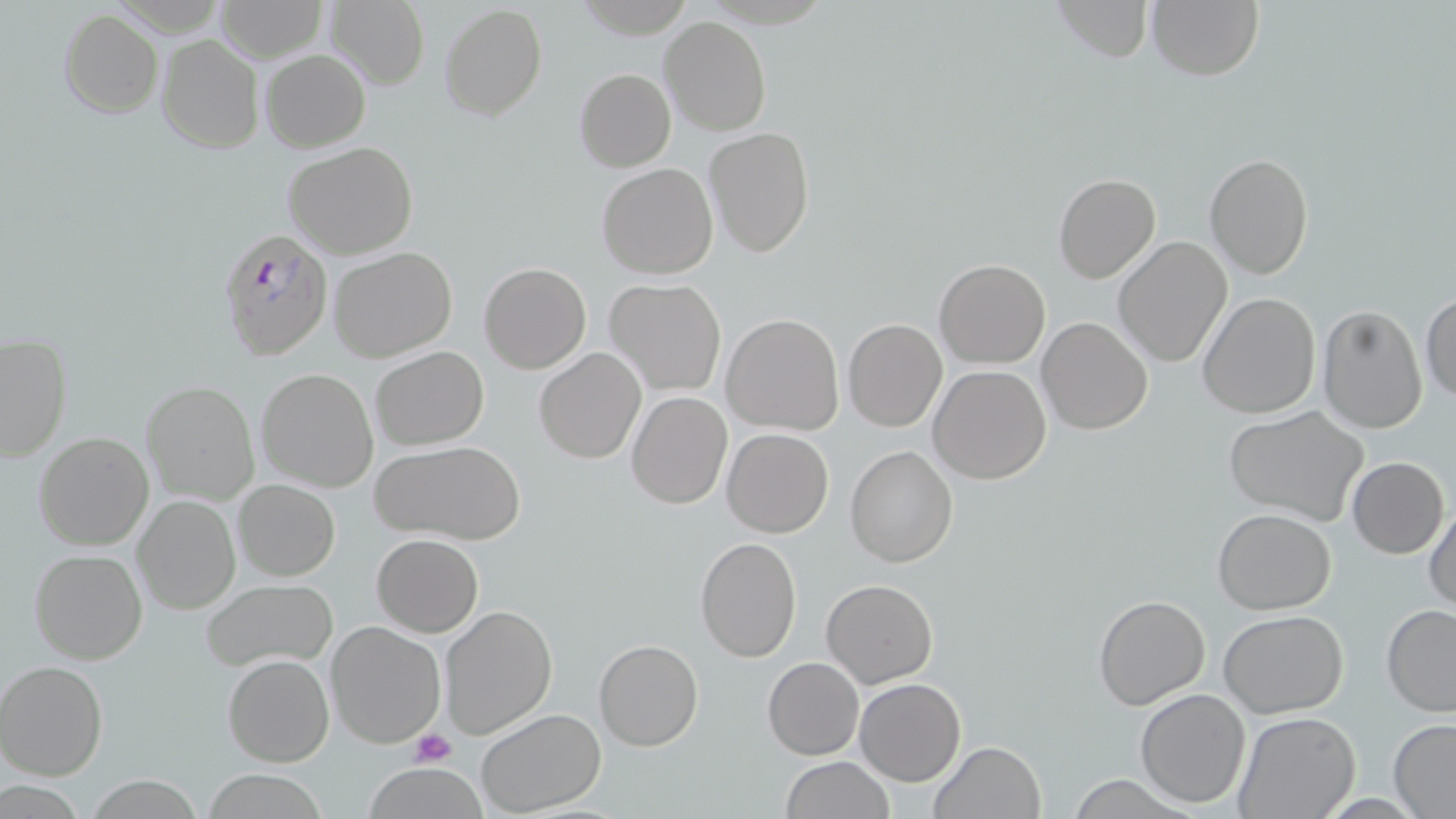

Summary:
  - Coordinate format: approximate bounding boxes as (x1, y1, x2, y2) in pixels
  - Uninfected red blood cell locations: (213, 0, 325, 60), (1050, 0, 1155, 63), (1146, 0, 1264, 81), (323, 1, 430, 88), (439, 3, 547, 122), (59, 9, 163, 118), (660, 16, 772, 136), (156, 35, 263, 154), (260, 48, 371, 152), (574, 68, 675, 173), (703, 127, 815, 260), (283, 141, 420, 260), (1205, 153, 1315, 280), (596, 164, 718, 280), (1053, 173, 1160, 283), (1112, 236, 1232, 367), (328, 247, 458, 363), (934, 259, 1051, 368), (479, 262, 591, 374), (604, 278, 726, 396), (1198, 292, 1321, 419), (1421, 292, 1455, 404), (1318, 305, 1428, 433), (721, 313, 844, 435), (1036, 316, 1153, 434), (843, 319, 947, 431), (1, 335, 72, 462), (371, 346, 489, 451), (534, 348, 646, 463), (928, 365, 1052, 483), (256, 368, 379, 493), (141, 382, 259, 505), (626, 391, 732, 509), (1225, 406, 1370, 527), (721, 427, 833, 537), (33, 431, 156, 551), (375, 440, 524, 547), (846, 446, 958, 566), (1347, 456, 1449, 558), (233, 479, 340, 582), (133, 494, 241, 616), (1424, 501, 1456, 615), (1213, 508, 1338, 614), (372, 534, 483, 636), (694, 536, 803, 662), (29, 547, 148, 665), (822, 577, 937, 688), (201, 579, 337, 672), (1093, 594, 1211, 711), (1381, 604, 1456, 715), (440, 605, 557, 739), (1219, 610, 1349, 717), (326, 621, 447, 749), (594, 639, 703, 751), (223, 654, 333, 767), (762, 657, 864, 760), (0, 660, 108, 781), (854, 679, 965, 786), (1135, 689, 1250, 806), (475, 708, 605, 816), (1233, 711, 1360, 818), (1387, 718, 1456, 816), (929, 740, 1048, 819), (780, 757, 893, 818), (360, 763, 491, 818), (203, 772, 326, 818)
  - Plasmodium falciparum-infected red blood cell locations: (219, 228, 332, 363)
  - Platelet locations: (409, 729, 456, 767)
  - Slide-level diagnosis: Plasmodium falciparum
  - Preparation: thin blood film
  - Field of view: single
  - Image size: 1456×819 pixels
  - Stain: May-Grünwald-Giemsa
  - Magnification: 1000x
  - Modality: optical microscopy